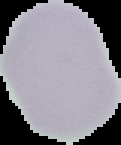
From a thin blood film. Image is 121×145 pixels. Segmented cell region on a black background. Result: negative for malaria parasites.